Report the malaria status of this cell.
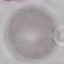

Uninfected.

Giemsa stain. Automatically extracted cell patch, resized to 64 × 64 pixels. Acquired by smartphone through the microscope eyepiece. Thin smear of blood.